Describe the morphology of the red blood cells.
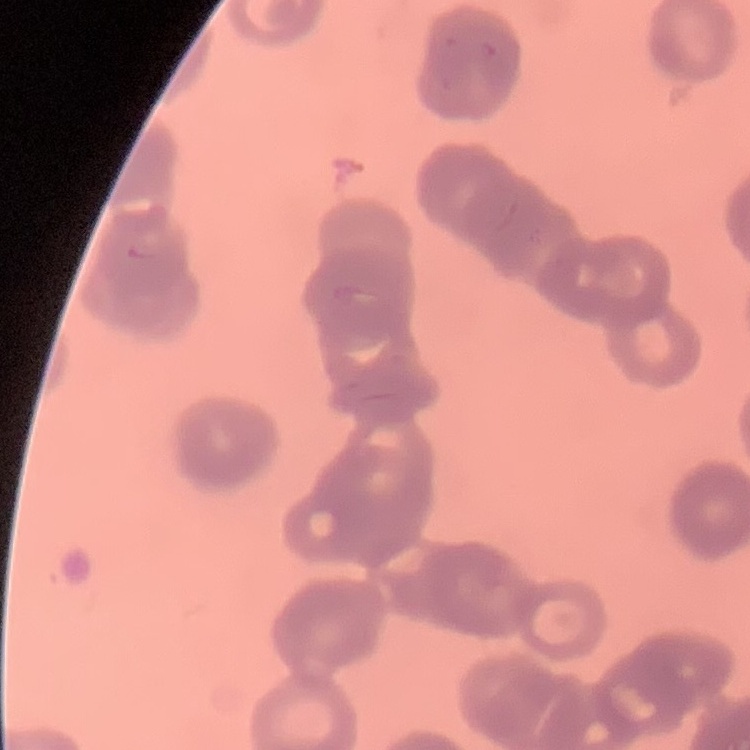

Rouleaux formation.

Summary:
  - Image type: square crop of a larger photomicrograph
  - Preparation: thin blood smear
  - Stain: Field's or Giemsa